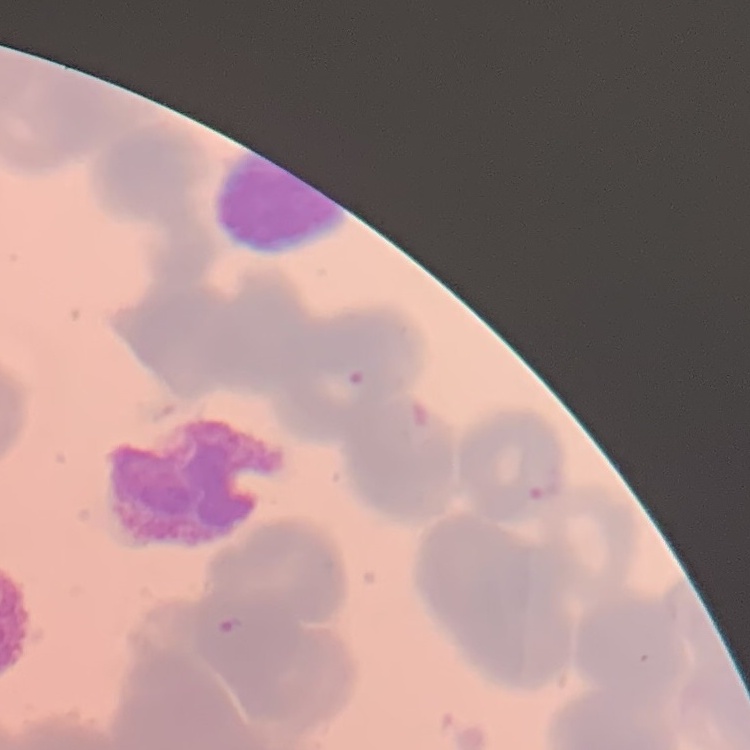
erythrocyte_morphology: rouleaux formation
stain: Field's or Giemsa
preparation: thin blood smear
image_type: one tile cut from a larger photomicrograph